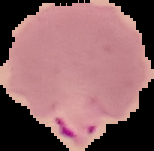
image type = segmented cell region on a black background
image size = 154×151 pixels
malaria status = parasitized
preparation = thin blood film